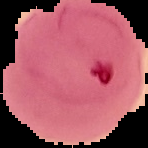
preparation = thin blood smear
image type = segmented cell region on a black background
image size = 148×148 pixels
malaria status = parasitized